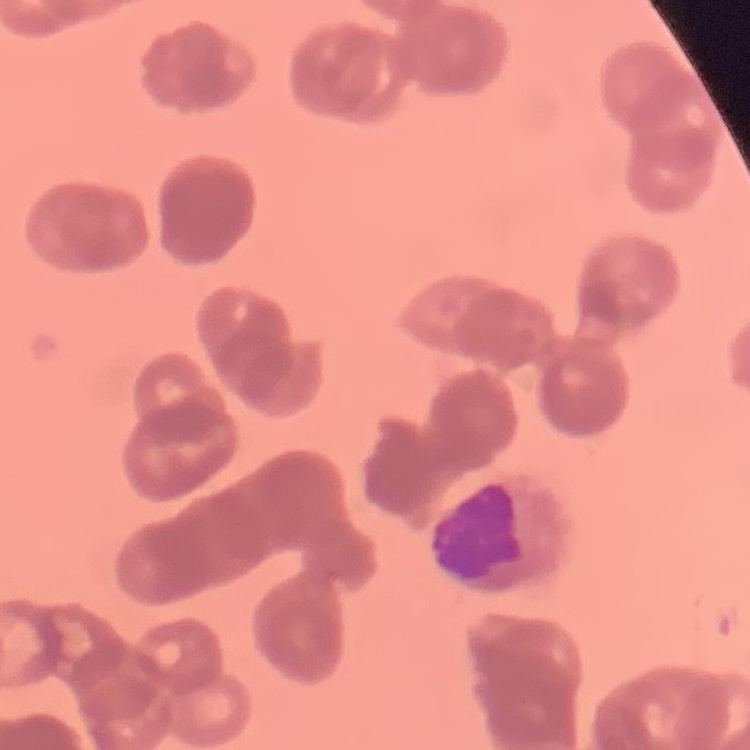
red blood cell morphology = rouleaux formation
preparation = thin peripheral smear
stain = Field's or Giemsa
image type = one tile cut from a larger photomicrograph